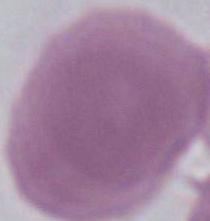

Summary:
  - Identification: red blood cell
  - Magnification: 1000x
  - Modality: micrograph